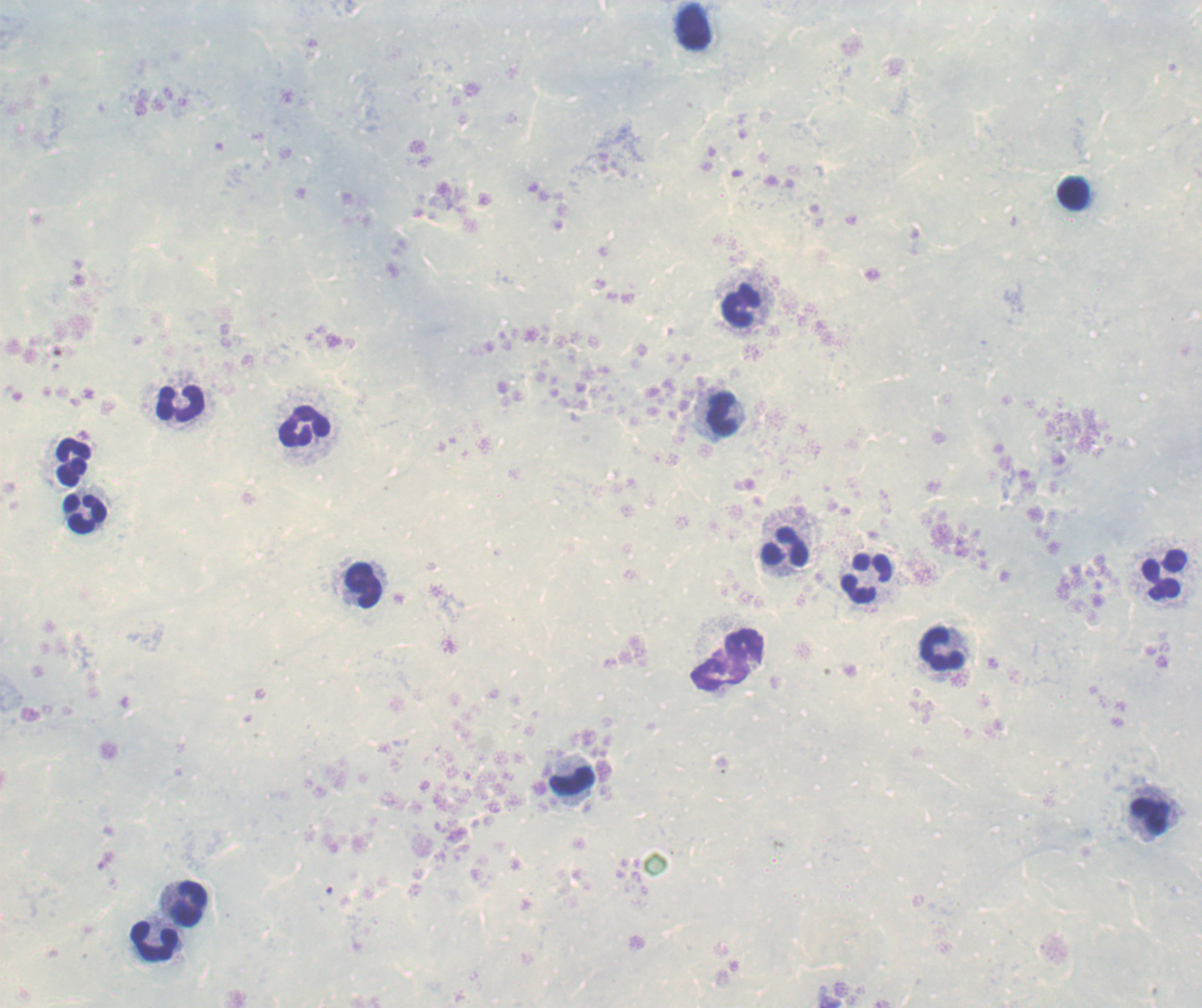

Approximate object centers, in pixels from the top-left corner. Leukocyte locations: (x=693, y=27), (x=1073, y=195), (x=742, y=306), (x=181, y=403), (x=723, y=416), (x=305, y=428), (x=74, y=463), (x=85, y=515), (x=784, y=547), (x=1164, y=575), (x=869, y=578), (x=363, y=586), (x=942, y=649), (x=726, y=661), (x=573, y=782), (x=1150, y=817), (x=188, y=902), (x=156, y=941). Image is 1202×1008 pixels. Previously used in an actual diagnosis. Captured at 100x magnification. Romanowsky stain. Background quality: unsatisfactory. Single field of view. Thick smear of blood. Result: no malaria parasites detected.